Assess this cell for malaria.
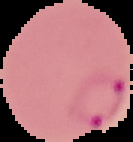

It is parasitized.

image size = 133×142 pixels
image type = segmented cell region on a black background
preparation = thin blood film